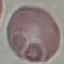

malaria_status: uninfected
stain: Giemsa
image_type: automatically extracted cell patch, resized to 64 × 64 pixels
capture: smartphone through the microscope eyepiece
preparation: thin blood smear